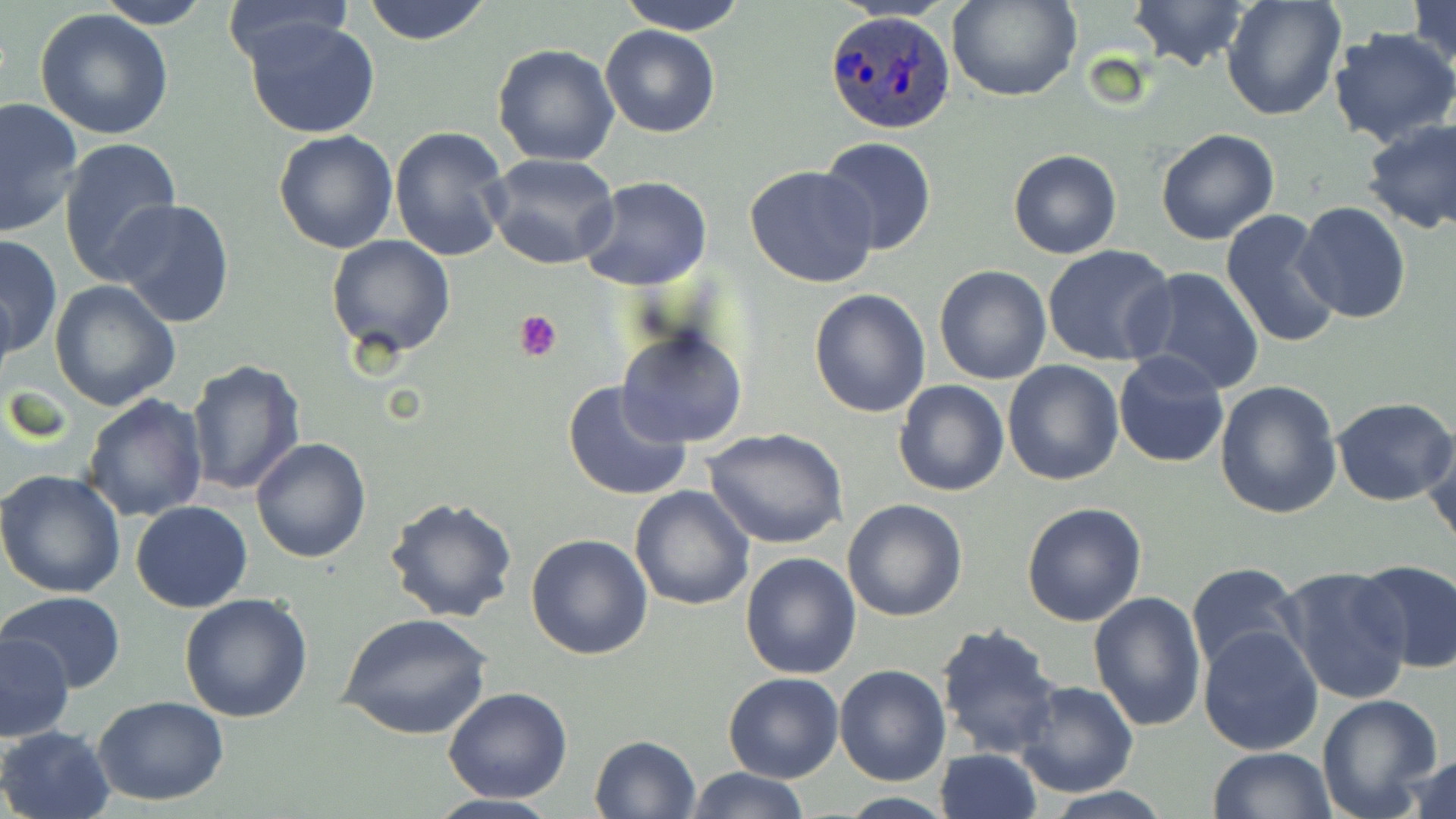
slide-level diagnosis = Plasmodium ovale
stain = May-Grünwald-Giemsa
modality = optical microscopy
platelet locations = approximate bounding boxes as (x1,y1)-(x2,y2) corner pairs in pixels: (514,309)-(563,361)
image size = 1456×819 pixels
field of view = single
magnification = 1000x
Plasmodium ovale-infected red blood cell locations = approximate bounding boxes as (x1,y1)-(x2,y2) corner pairs in pixels: (824,9)-(955,134)
uninfected red blood cell locations = approximate bounding boxes as (x1,y1)-(x2,y2) corner pairs in pixels: (361,0)-(494,46), (616,0)-(749,35), (948,0)-(1079,102), (1129,0)-(1249,73), (1221,0)-(1346,120), (1407,0)-(1456,74), (94,1)-(210,30), (220,1)-(355,68), (35,9)-(174,141), (244,17)-(380,140), (600,24)-(720,138), (1328,28)-(1456,147), (492,44)-(620,166), (0,96)-(85,236), (1361,117)-(1456,233), (388,126)-(512,264), (1155,129)-(1280,246), (273,130)-(399,254), (60,136)-(182,286), (819,137)-(937,256), (1007,150)-(1122,259), (486,153)-(620,271), (745,164)-(879,288), (578,175)-(713,291), (109,198)-(236,330), (1294,201)-(1412,324), (1220,208)-(1343,349), (1,232)-(62,357), (326,234)-(456,360), (1042,244)-(1177,368), (934,265)-(1051,384), (1128,266)-(1266,398), (50,280)-(182,410), (809,288)-(931,417), (616,323)-(748,450), (1113,350)-(1230,467), (186,358)-(308,497), (1003,361)-(1124,485), (563,378)-(695,502), (894,380)-(1010,498), (1214,380)-(1343,520), (81,392)-(208,523), (1331,396)-(1456,506), (703,427)-(849,549), (1419,429)-(1455,547), (250,437)-(372,565), (0,469)-(127,596), (629,485)-(756,611), (385,495)-(518,623), (842,499)-(968,622), (131,501)-(253,613), (1021,502)-(1149,627), (525,534)-(653,660), (739,551)-(863,680), (1353,560)-(1456,673), (1185,562)-(1303,679), (1275,565)-(1414,707), (1087,590)-(1207,731), (3,593)-(127,691), (179,593)-(315,722), (340,611)-(493,740), (935,622)-(1064,760), (1198,625)-(1324,755), (1,634)-(74,741), (835,664)-(952,786), (723,673)-(845,784), (1015,680)-(1138,796), (443,687)-(573,803), (1315,694)-(1444,819), (95,696)-(229,805), (0,725)-(115,819), (589,735)-(701,819), (935,748)-(1042,819), (1206,748)-(1334,819), (1403,752)-(1455,819), (686,766)-(808,819), (421,793)-(567,819)
preparation = thin blood film